State which parasite is depicted.
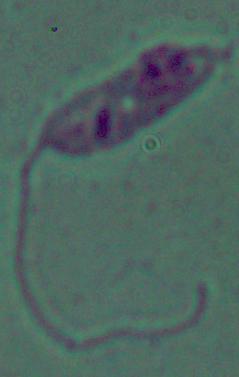
This is Leishmania.

Captured at 1000x magnification. Micrograph.